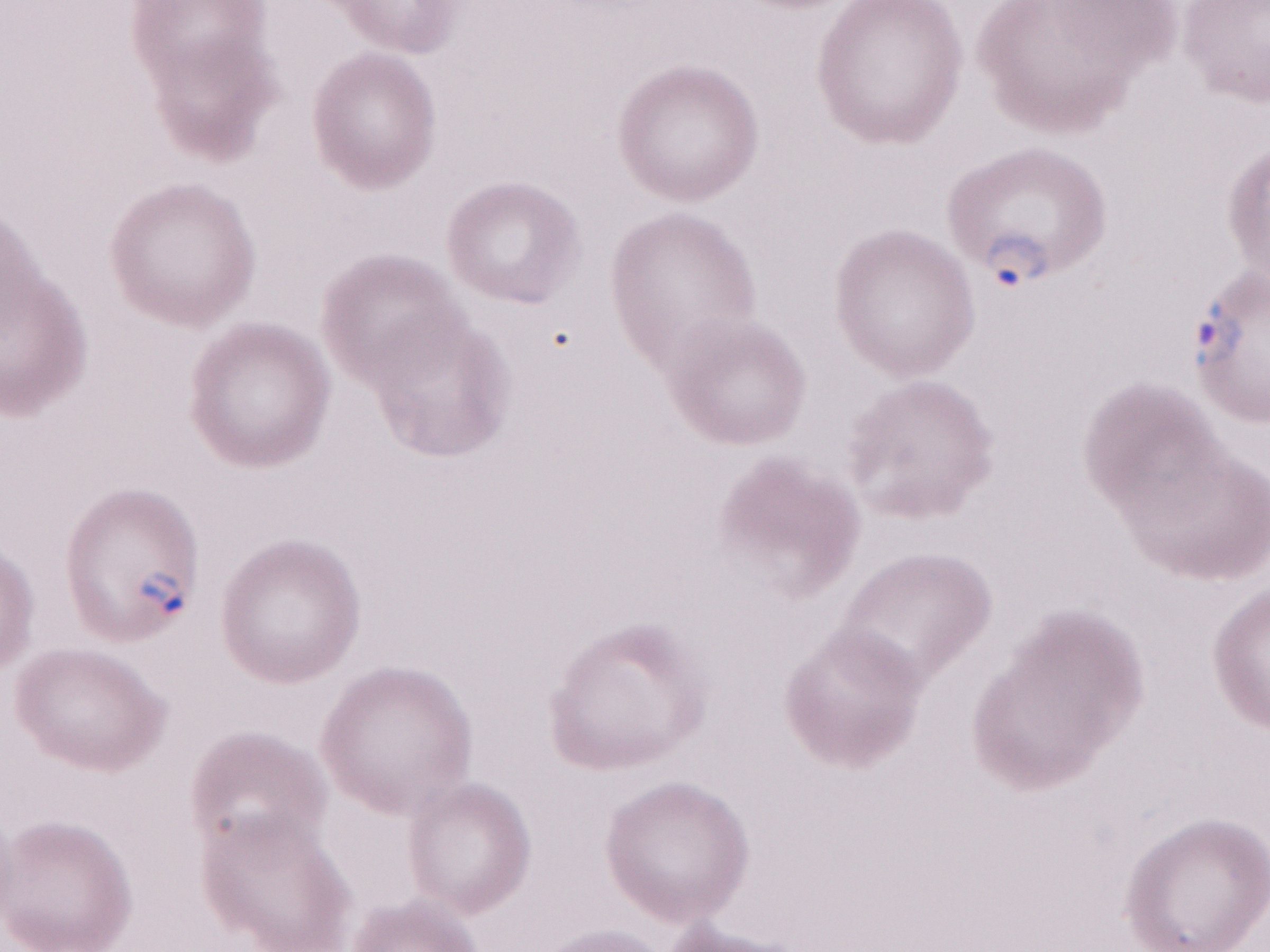

May-Grünwald-Giemsa stain. Image is 1270×952 pixels. 1,000x magnification. Olympus BX43 microscope and DP73 digital camera. Single field of view. Patient diagnosis: malaria infection. Thin peripheral-blood smear.